Identify the parasite.
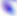
Toxoplasma gondii.

Summary:
  - Magnification: 400x
  - Modality: photomicrograph